Locate every blood parasite and identify its species.
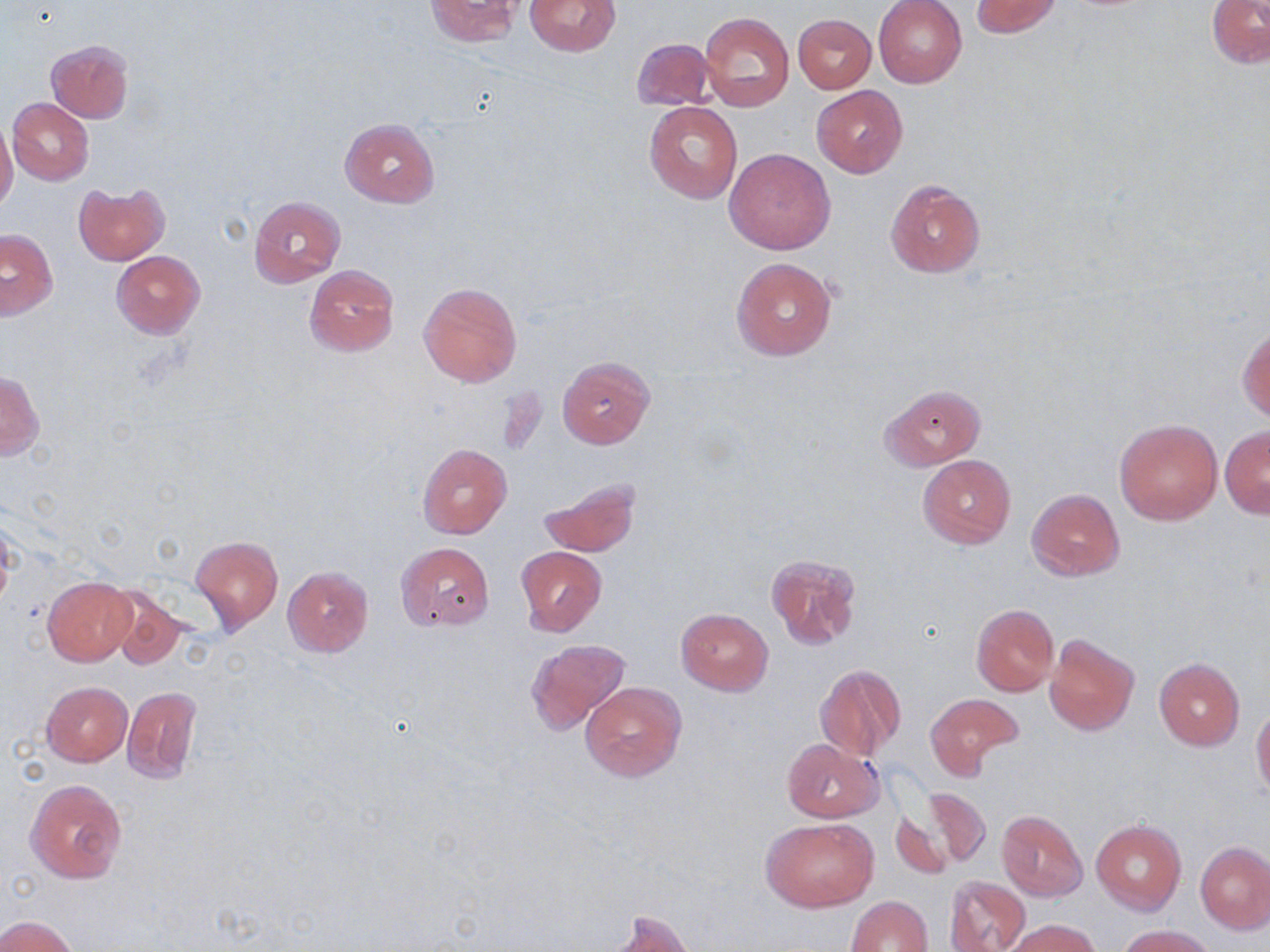

No blood parasites seen.

Approximate bounding boxes as (x1, y1, x2, y2) in pixels. Uninfected red blood cell locations: (525, 0, 621, 56), (970, 0, 1061, 38), (1207, 0, 1270, 69), (423, 1, 524, 46), (873, 1, 967, 88), (699, 11, 794, 110), (793, 13, 876, 93), (632, 38, 718, 112), (44, 39, 135, 123), (811, 85, 908, 178), (8, 97, 94, 185), (644, 102, 743, 204), (339, 117, 440, 208), (0, 120, 18, 214), (725, 148, 835, 255), (885, 180, 984, 278), (73, 184, 169, 265), (249, 196, 346, 287), (1, 228, 57, 320), (111, 250, 206, 339), (731, 257, 839, 360), (306, 264, 399, 358), (418, 283, 521, 388), (1239, 325, 1269, 424), (557, 356, 655, 450), (0, 373, 44, 461), (880, 384, 985, 469), (1114, 418, 1223, 525), (1220, 426, 1269, 517), (417, 443, 512, 540), (918, 455, 1016, 548), (539, 479, 640, 557), (1026, 488, 1124, 581), (0, 515, 16, 613), (191, 535, 283, 633), (396, 542, 494, 631), (516, 546, 605, 636), (766, 554, 862, 651), (282, 566, 374, 657), (43, 578, 137, 666), (109, 590, 188, 672), (971, 604, 1059, 696), (676, 608, 773, 695), (1045, 634, 1139, 735), (526, 638, 630, 734), (1153, 657, 1246, 751), (814, 663, 907, 763), (40, 681, 133, 766), (580, 682, 687, 780), (122, 685, 203, 784), (924, 692, 1023, 778), (1251, 708, 1270, 798), (781, 738, 884, 822), (26, 780, 126, 884), (921, 787, 991, 867), (890, 808, 955, 882), (996, 809, 1088, 901), (759, 817, 879, 912), (1091, 819, 1186, 916), (1196, 841, 1270, 934), (944, 874, 1031, 952), (846, 895, 932, 952), (603, 911, 694, 952), (0, 914, 81, 952), (1003, 918, 1101, 952), (1118, 924, 1215, 952). Slide-level diagnosis: negative for blood parasites. May-Grünwald-Giemsa stain. Thin blood film. Image is 1270×952 pixels. Captured at 1000x magnification. Optical microscopy. Single field of view.